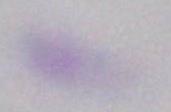

Photomicrograph. 1000x magnification. Toxoplasma gondii is seen.